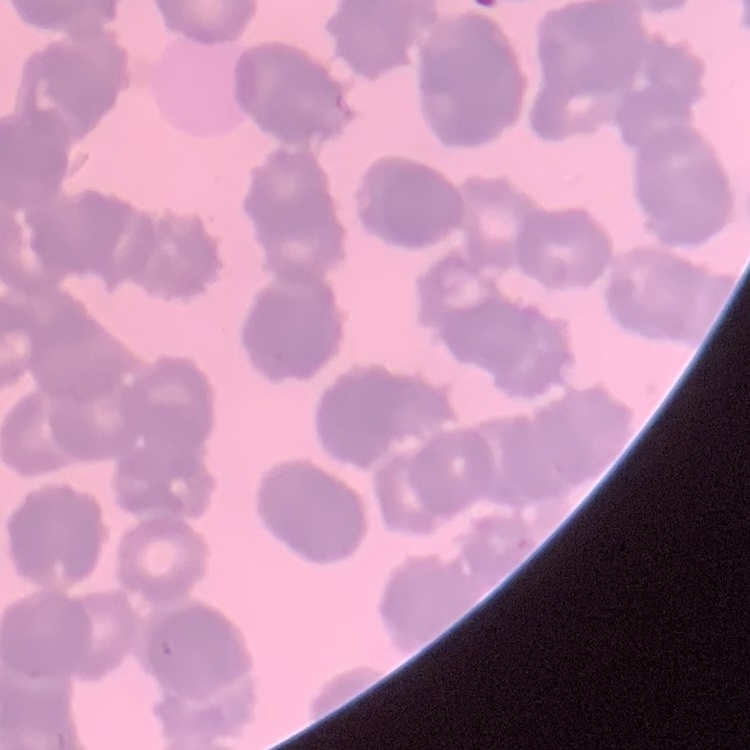
Summary:
  - Erythrocyte morphology: rouleaux formation
  - Image type: square crop of a larger photomicrograph
  - Preparation: thin blood film
  - Stain: Field's or Giemsa